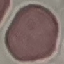 Malaria status: uninfected. Thin blood film. Cell patch, automatically extracted from a larger field of view and resized to 64 × 64 pixels. Giemsa stain. Photographed with a smartphone camera at the microscope eyepiece.